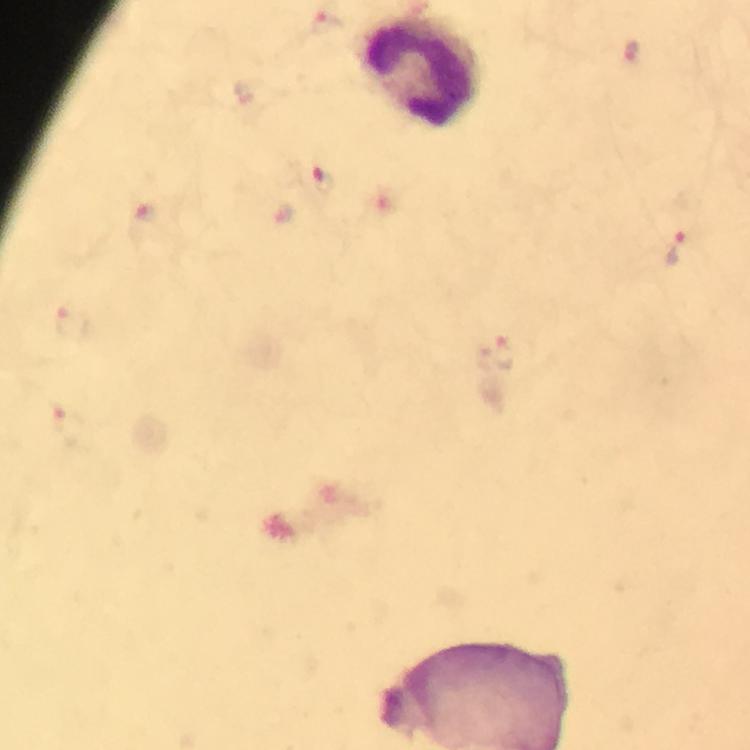

magnification = 100x
stain = Giemsa
capture = smartphone camera through the microscope
image size = 750×750 pixels
preparation = thick blood smear
cropped from = one field of view
immersion oil = used
malaria parasite locations = approximate centers as {x, y} in pixels: {324, 22}, {631, 51}, {324, 181}, {141, 219}, {678, 247}, {73, 324}, {495, 354}
context = from a diagnostic examination for malaria